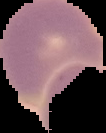

Summary:
  - Image size: 106×133 pixels
  - Malaria status: uninfected
  - Image type: segmented cell region on a black background
  - Preparation: thin blood smear